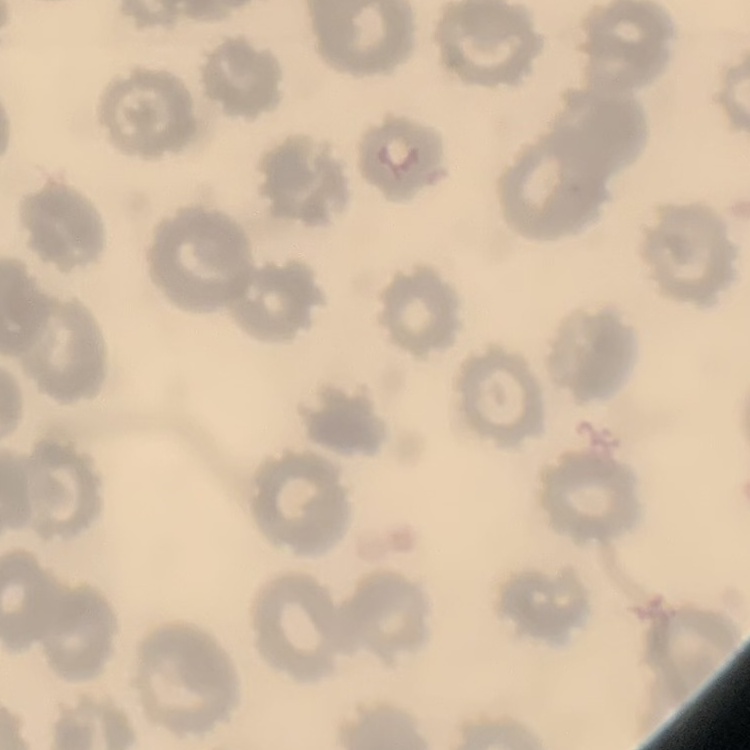
The red blood cells exhibit no rouleaux formation. Square crop of a larger photomicrograph. Thin peripheral smear. Stained with either Field's or Giemsa.